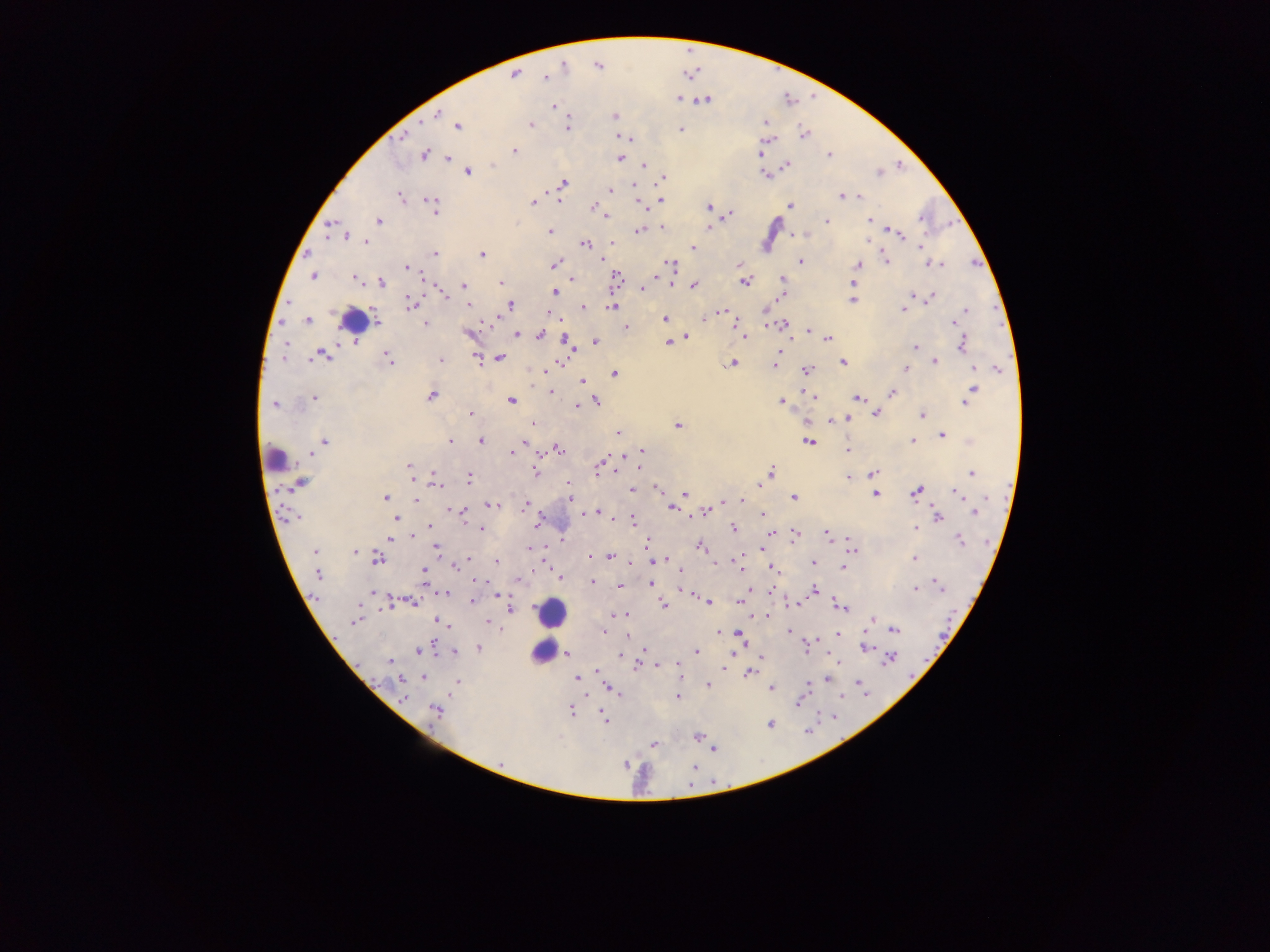

Approximate centers as x y in pixels.
Summary:
  - Malaria parasite locations: 563 65; 598 66; 513 74; 545 77; 678 98; 704 99; 552 106; 438 114; 614 115; 765 121; 458 125; 529 125; 567 128; 680 129; 803 134; 403 136; 619 136; 630 138; 766 140; 514 151; 425 154; 759 154; 828 154; 447 158; 619 158; 785 164; 644 165; 466 171; 877 172; 765 174; 662 177; 563 183; 633 186; 561 187; 609 190; 842 196; 860 196; 401 197; 559 200; 431 201; 532 202; 661 202; 640 203; 789 205; 592 206; 433 207; 709 207; 728 214; 605 216; 920 217; 869 219; 826 220; 379 221; 331 226; 663 227; 709 227; 639 230; 549 231; 889 231; 897 232; 805 233; 790 234; 344 235; 365 241; 868 241; 612 242; 584 243; 693 247; 920 247; 434 253; 481 254; 600 258; 886 261; 800 262; 930 263; 937 263; 554 264; 671 264; 739 265; 857 265; 407 267; 313 275; 616 277; 355 278; 656 278; 783 278; 570 279; 669 281; 743 281; 380 282; 853 282; 501 283; 464 285; 693 285; 640 288; 554 292; 781 295; 913 295; 444 296; 929 298; 851 300; 409 302; 467 304; 509 304; 614 306; 583 307; 903 309; 765 310; 721 311; 964 311; 550 315; 706 317; 958 318; 490 319; 665 319; 702 319; 765 319; 307 320; 732 320; 954 322; 377 323; 425 323; 767 323; 784 323; 624 327; 809 329; 468 332; 739 332; 517 334; 539 334; 793 335; 743 336; 687 337; 828 338; 567 341; 595 342; 285 343; 668 343; 962 343; 915 347; 570 349; 323 354; 777 356; 282 358; 476 358; 498 358; 388 359; 439 359; 842 361; 933 361; 731 362; 559 363; 774 365; 973 367; 806 369; 996 369; 544 370; 905 370; 614 374; 582 381; 973 390; 551 392; 805 392; 892 393; 810 395; 431 396; 314 397; 814 397; 858 398; 511 400; 595 400; 781 401; 965 402; 274 404; 575 406; 875 413; 471 414; 923 415; 847 418; 828 421; 533 425; 678 426; 618 432; 942 434; 449 440; 912 440; 480 441; 324 442; 808 442; 522 446; 558 449; 846 449; 642 450; 511 453; 311 454; 619 457; 601 464; 409 465; 640 467; 597 470; 613 471; 534 472; 770 472; 873 473; 971 473; 411 477; 433 477; 468 477; 847 478; 299 483; 568 483; 436 486; 758 486; 655 487; 631 490; 915 491; 958 492; 684 493; 875 494; 385 497; 794 497; 569 498; 416 500; 743 500; 724 502; 493 504; 524 505; 711 505; 670 507; 453 509; 706 511; 463 512; 584 512; 597 512; 975 512; 602 514; 761 516; 937 516; 295 517; 613 517; 395 519; 631 522; 536 523; 429 526; 481 528; 732 528; 916 528; 769 533; 793 534; 407 538; 826 539; 849 539; 390 540; 959 540; 647 542; 436 546; 699 547; 528 549; 761 550; 852 551; 315 552; 354 552; 609 556; 377 558; 469 558; 739 558; 915 558; 496 561; 659 562; 713 563; 812 563; 456 564; 633 566; 740 567; 843 567; 679 568; 771 568; 423 571; 317 573; 560 577; 425 579; 475 581; 590 581; 649 583; 935 583; 619 585; 940 586; 749 588; 680 590; 813 590; 915 590; 770 591; 372 592; 687 592; 445 593; 496 595; 743 597; 472 600; 740 600; 413 601; 708 601; 390 602; 794 603; 664 604; 837 605; 841 606; 510 610; 765 614; 616 615; 356 620; 437 620; 872 620; 487 621; 444 624; 893 629; 603 630; 788 631; 718 632; 738 634; 837 635; 741 641; 479 647; 864 647; 805 648; 644 649; 418 651; 733 651; 696 652; 454 653; 567 654; 620 654; 761 656; 890 657; 836 658; 390 662; 677 664; 656 665; 636 666; 726 668; 596 670; 752 672; 423 676; 679 676; 576 677; 401 678; 826 678; 858 680; 456 682; 861 683; 707 685; 772 688; 805 688; 612 689; 615 691; 677 696; 401 697; 798 700; 570 710; 435 711; 601 712; 604 719; 770 723; 697 736; 654 744; 713 748; 500 763; 625 763; 694 766
  - Leukocyte locations: 354 321; 274 459; 552 612; 540 652
  - Image size: 1270×952 pixels
  - Preparation: thick blood film
  - Country: Ghana
  - Capture: mobile-phone photograph through a microscope
  - Field of view: single